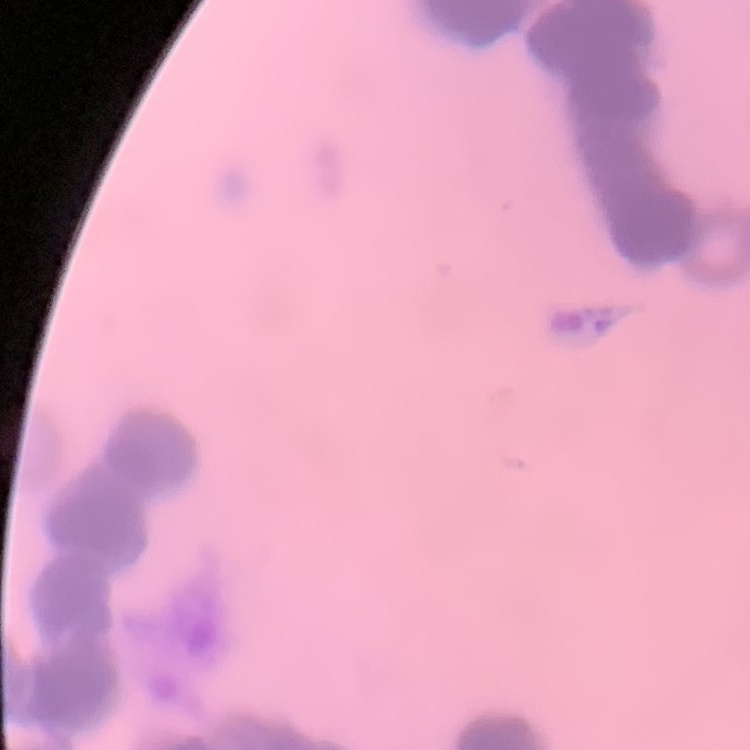
Summary:
  - Erythrocyte morphology: rouleaux formation
  - Preparation: thin peripheral smear
  - Stain: Field's or Giemsa
  - Image type: square crop of a larger photomicrograph